State which parasite is depicted.
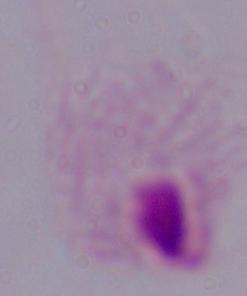

This is a trichomonad.

Summary:
  - Modality: micrograph
  - Magnification: 1000x